Point out leukocytes.
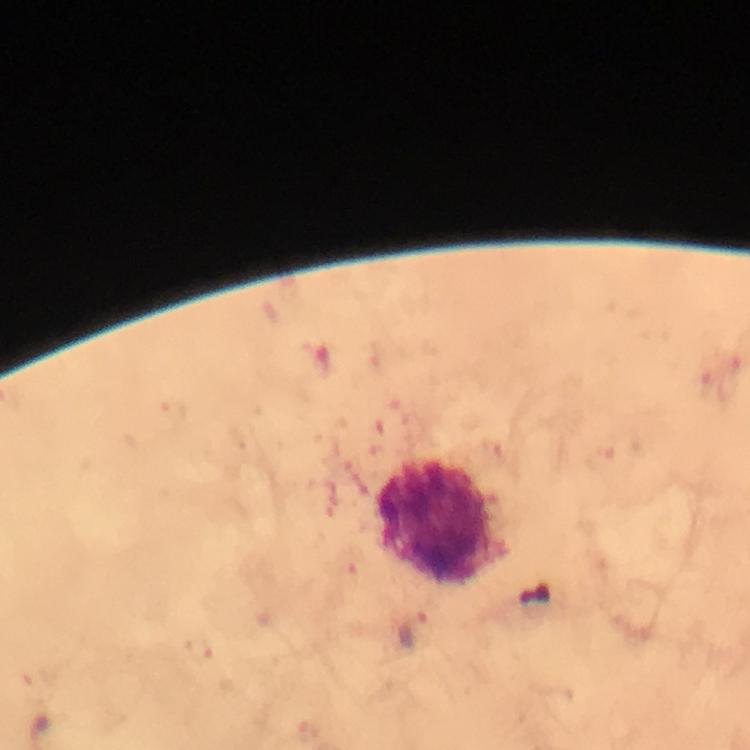
Approximate centers as {x, y} in pixels.
Leukocytes: {440, 522}.

magnification = 100x
image size = 750×750 pixels
capture = smartphone mounted on the microscope
stain = Giemsa
preparation = thick blood smear
malaria parasite locations = approximate centers as {x, y} in pixels: {413, 631}
context = from a diagnostic examination for malaria
immersion oil = applied
cropped from = a single field of view